State the blood parasite species.
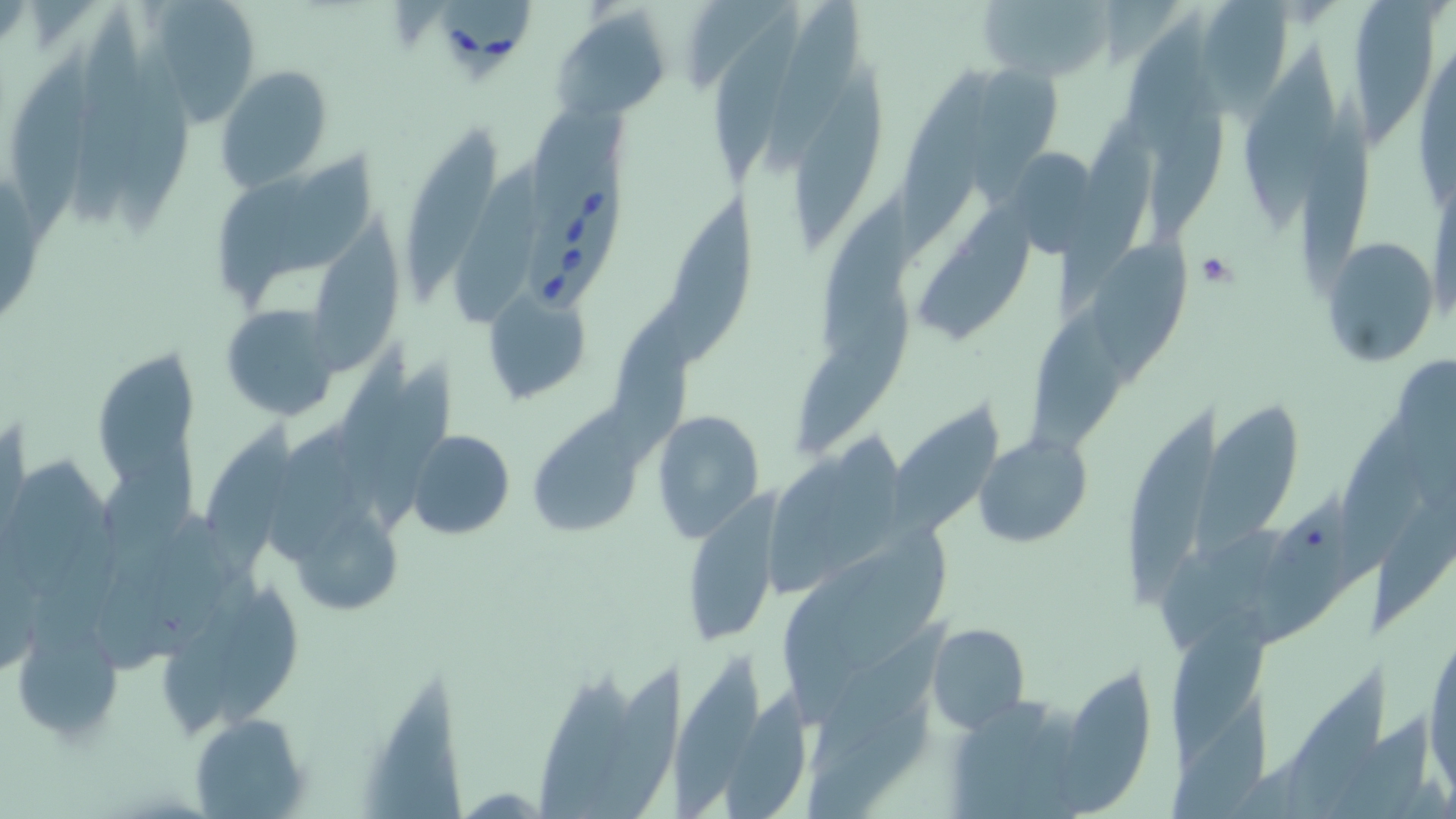

Babesia divergens.

Approximate bounding boxes as (x1,y1)-(x2,y2) corner pairs in pixels. Uninfected red blood cell locations: (137,0)-(265,121), (685,0)-(789,95), (976,0)-(1117,81), (1197,0)-(1296,107), (762,1)-(862,179), (1358,2)-(1438,151), (64,6)-(156,231), (707,7)-(797,188), (554,8)-(671,121), (1414,31)-(1456,217), (110,38)-(188,236), (2,42)-(95,255), (1238,46)-(1343,240), (980,57)-(1062,201), (217,65)-(334,192), (893,68)-(996,266), (785,69)-(889,254), (1146,81)-(1228,237), (1297,92)-(1381,290), (404,124)-(506,303), (1052,124)-(1154,315), (273,154)-(378,282), (454,172)-(540,331), (217,174)-(312,304), (661,197)-(749,373), (917,202)-(1036,349), (311,211)-(399,375), (1092,234)-(1189,384), (1320,238)-(1442,366), (484,288)-(594,407), (602,291)-(707,463), (797,294)-(915,454), (222,305)-(339,420), (89,343)-(201,505), (883,402)-(1006,547), (1195,404)-(1304,560), (533,409)-(640,539), (651,410)-(765,541), (1119,410)-(1226,605), (1336,410)-(1427,583), (264,419)-(367,562), (199,423)-(298,578), (408,430)-(514,541), (974,433)-(1093,548), (686,487)-(785,645), (1254,494)-(1360,645), (1367,496)-(1456,636), (293,507)-(399,613), (217,590)-(304,723), (1165,610)-(1274,768), (10,617)-(121,744), (925,622)-(1030,732), (1424,622)-(1456,796), (665,658)-(770,819), (584,664)-(687,819), (1061,674)-(1157,816), (358,676)-(466,818), (723,686)-(820,819), (189,711)-(310,819). Platelet locations: (1193,253)-(1240,293). Babesia divergens-infected red blood cell locations: (434,0)-(534,83), (523,156)-(628,320). Single field of view. Thin blood film. Optical microscopy. May-Grünwald-Giemsa-stained preparation. Image is 1456×819 pixels. 1000x magnification.